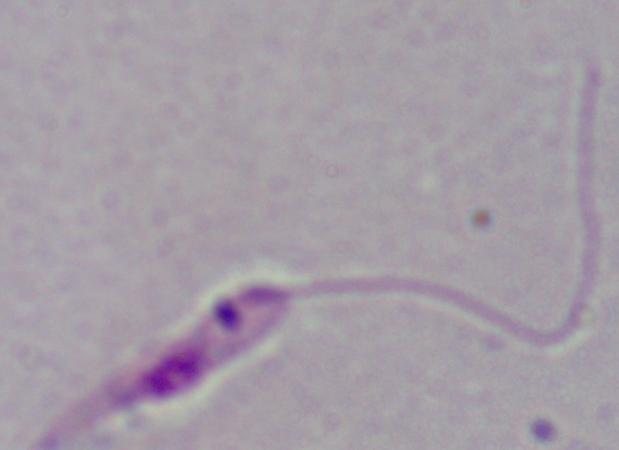

Summary:
  - Modality: micrograph
  - Identification: Leishmania
  - Magnification: 1000x